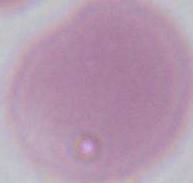

magnification = 1000x
identification = erythrocyte
modality = micrograph